Report the malaria status of this cell.
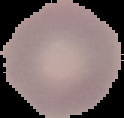

It is uninfected.

image size = 124×118 pixels
preparation = thin blood smear
image type = segmented cell region with the area outside set to black